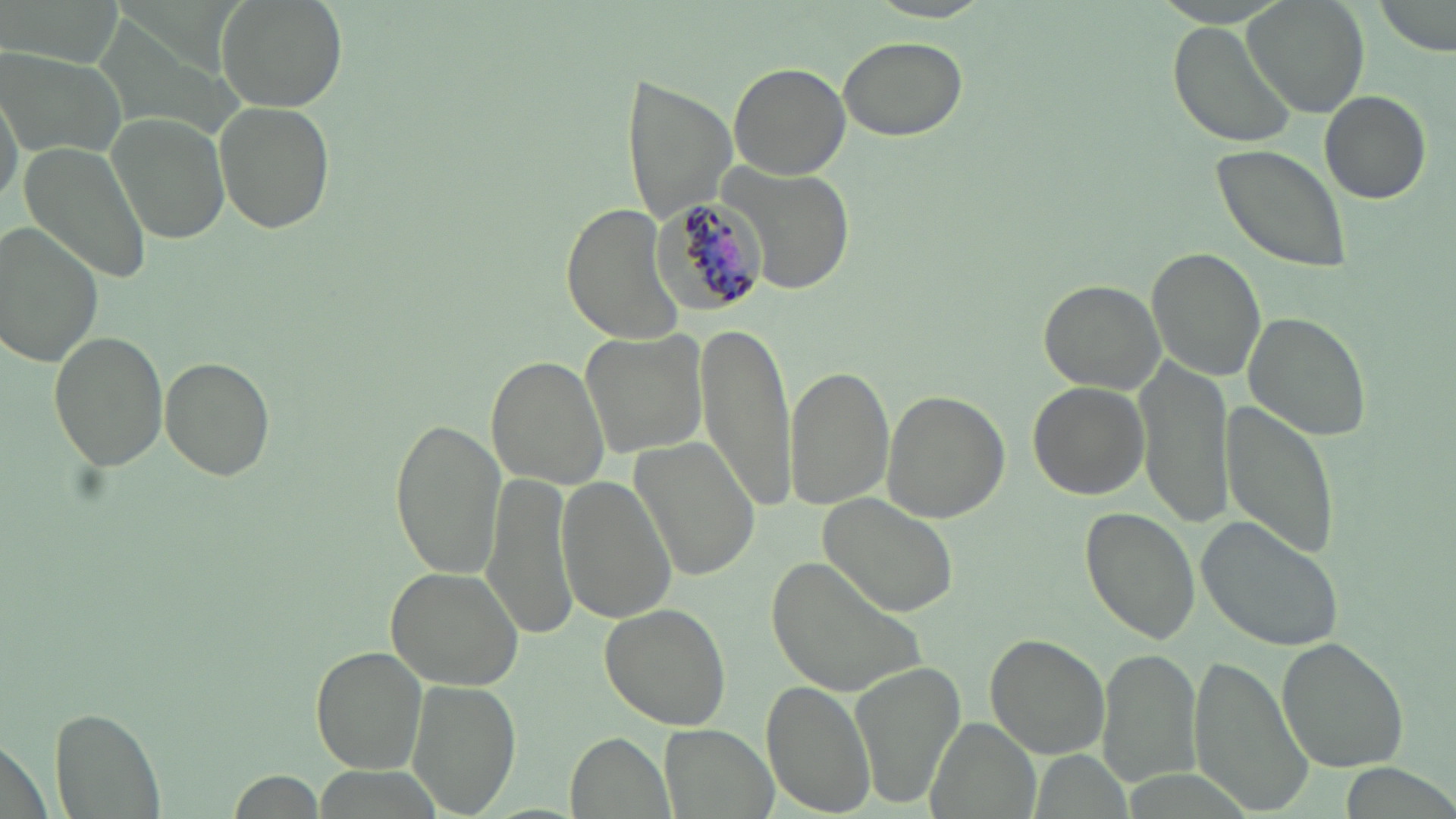 Approximate bounding boxes as (x1,y1)-(x2,y2) corner pairs in pixels. Uninfected red blood cell locations: (216,0)-(347,114), (1243,0)-(1370,117), (1373,0)-(1452,53), (865,1)-(996,23), (1167,23)-(1296,148), (838,34)-(968,141), (2,44)-(128,160), (729,62)-(850,179), (620,71)-(737,225), (1320,90)-(1431,203), (213,99)-(336,235), (106,110)-(231,246), (17,138)-(152,288), (1209,143)-(1353,274), (718,158)-(859,295), (563,204)-(691,345), (1,220)-(107,367), (1149,248)-(1267,380), (1037,279)-(1168,395), (1243,311)-(1372,442), (695,319)-(798,516), (47,328)-(169,472), (579,330)-(707,460), (158,355)-(276,481), (486,356)-(612,488), (1136,357)-(1234,526), (786,362)-(895,512), (1028,381)-(1148,499), (880,390)-(1009,521), (1220,397)-(1341,557), (389,415)-(505,580), (629,436)-(760,582), (481,472)-(579,641), (555,474)-(679,623), (814,493)-(960,619), (1082,508)-(1200,643), (1197,514)-(1346,653), (770,552)-(931,698), (384,566)-(523,691), (599,601)-(734,730), (986,635)-(1110,758), (1277,636)-(1407,770), (311,646)-(428,772), (1095,648)-(1200,788), (1188,653)-(1312,814), (848,661)-(967,807), (408,679)-(519,814), (760,682)-(876,815), (53,706)-(165,819), (924,717)-(1039,819), (658,722)-(783,819), (570,734)-(671,818), (1337,762)-(1456,818), (228,770)-(326,817). Plasmodium malariae-infected red blood cell locations: (651,196)-(770,311). Slide-level diagnosis: Plasmodium malariae. Single field of view. Light microscopy. May-Grünwald-Giemsa-stained preparation. Captured at 1000x magnification. Thin blood smear. Image is 1456×819 pixels.